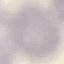 Malaria status: uninfected. Thin blood film. Photographed with a smartphone camera at the microscope eyepiece. Giemsa stain. Cell patch, automatically extracted from a larger field of view and resized to 64 × 64 pixels.